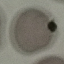 Malaria status: uninfected. Thin blood smear. Cell patch, automatically extracted from a larger field of view and resized to 64 × 64 pixels. Giemsa-stained preparation. Photographed with a smartphone camera at the microscope eyepiece.